Identify the cell.
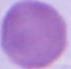
An erythrocyte.

Captured at 1000x magnification. Micrograph.